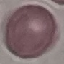

Summary:
  - Malaria status: uninfected
  - Stain: Giemsa
  - Image type: automatically extracted cell patch, resized to 64 × 64 pixels
  - Preparation: thin blood smear
  - Capture: smartphone camera at the microscope eyepiece